Identify the cell.
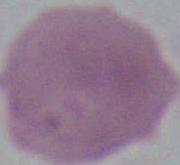

This is an erythrocyte.

modality: micrograph
magnification: 1000x